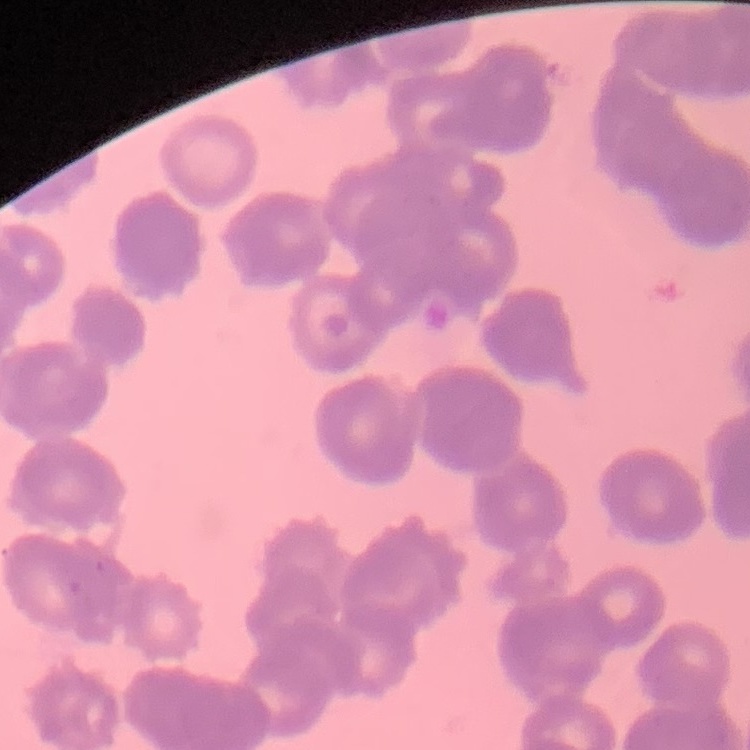

erythrocyte morphology = rouleaux formation
preparation = thin blood film
image type = square crop of a larger photomicrograph
stain = Field's or Giemsa